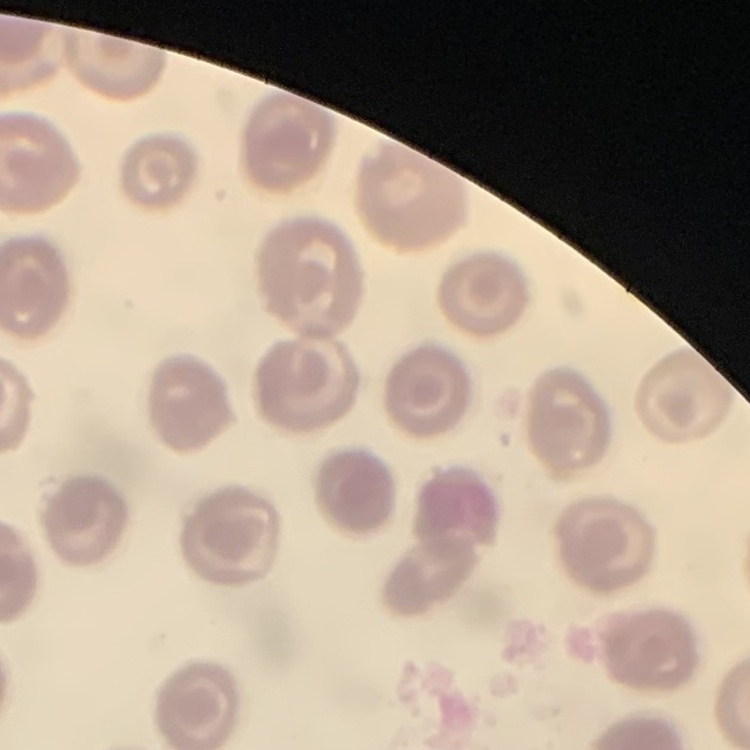
erythrocyte morphology = no rouleaux formation
stain = Field's or Giemsa
image type = one tile cut from a larger photomicrograph
preparation = thin peripheral smear